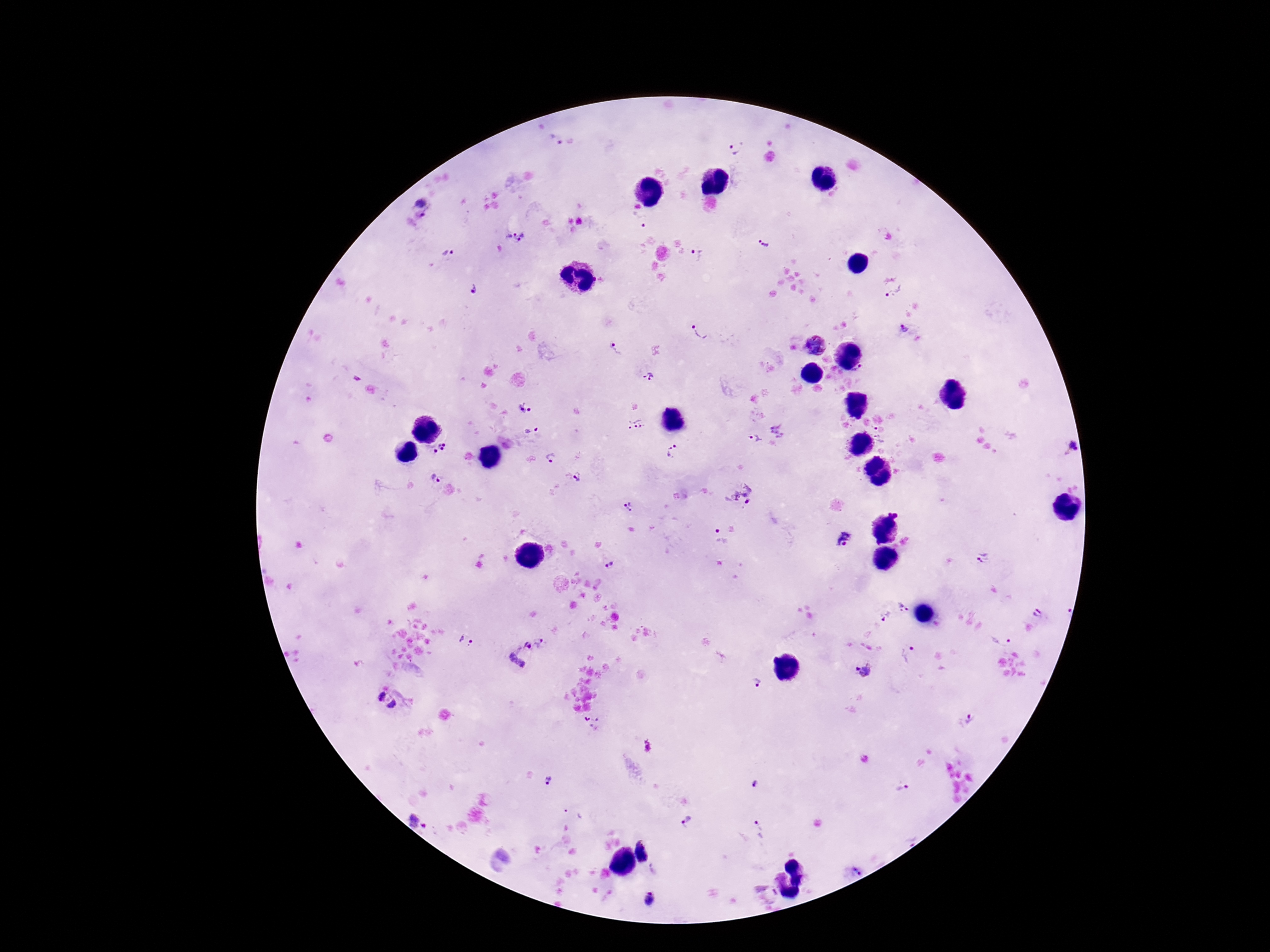

Approximate centers as [x, y] in pixels.
Summary:
  - Plasmodium parasite locations: [555, 141], [735, 148], [422, 201], [421, 217], [638, 219], [510, 234], [523, 238], [764, 242], [446, 254], [698, 254], [473, 289], [895, 293], [904, 328], [700, 332], [618, 349], [861, 373], [649, 378], [525, 407], [634, 425], [879, 429], [778, 430], [532, 432], [880, 439], [753, 440], [439, 444], [444, 445], [1072, 446], [442, 449], [435, 451], [674, 452], [551, 458], [437, 477], [578, 477], [742, 495], [629, 507], [718, 537], [846, 540], [983, 558], [610, 565], [903, 607], [1038, 613], [884, 616], [1001, 637], [466, 641], [539, 643], [527, 646], [910, 654], [518, 658], [865, 670], [755, 683], [380, 695], [393, 705], [969, 718], [549, 782], [754, 786], [903, 787], [414, 820], [687, 820], [424, 826], [758, 830], [647, 851], [854, 870], [649, 898]
  - Capture: smartphone camera through the microscope eyepiece
  - Field of view: single
  - Stain: Giemsa
  - Magnification: 100x
  - Preparation: thick blood film
  - Patient malaria status: infected
  - Image size: 1270×952 pixels